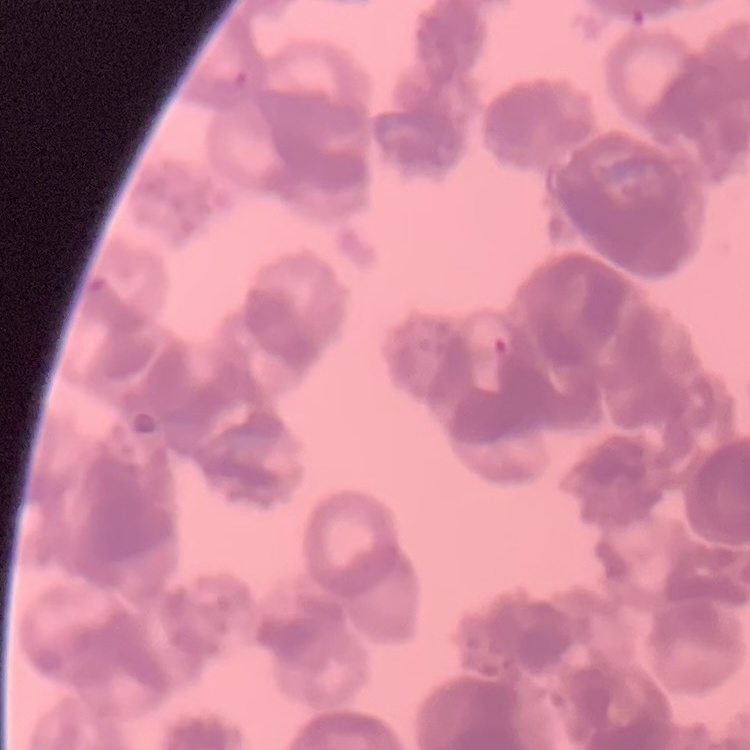 The erythrocytes exhibit rouleaux formation. Thin blood film. Field's or Giemsa stain. One tile cut from a larger photomicrograph.